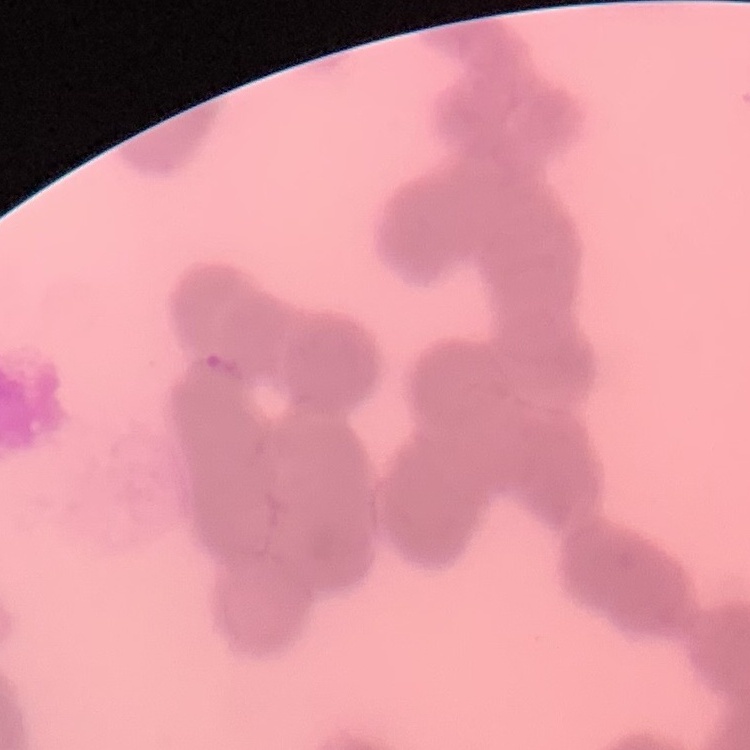
Summary:
  - Erythrocyte morphology: rouleaux formation
  - Preparation: thin blood smear
  - Stain: Field's or Giemsa
  - Image type: square crop of a larger photomicrograph